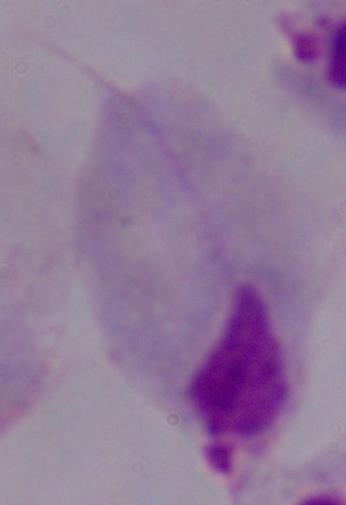

A trichomonad is shown. 1000x magnification. Micrograph.